State which cell type is depicted.
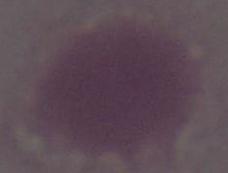
This is an erythrocyte.

Captured at 1000x magnification. Photomicrograph.